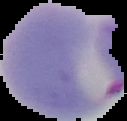

Cell region segmented out of the field of view; the surrounding area is masked to black. Image is 127×121 pixels. Result: Plasmodium parasites detected. From a thin blood smear.